Evaluate for malaria.
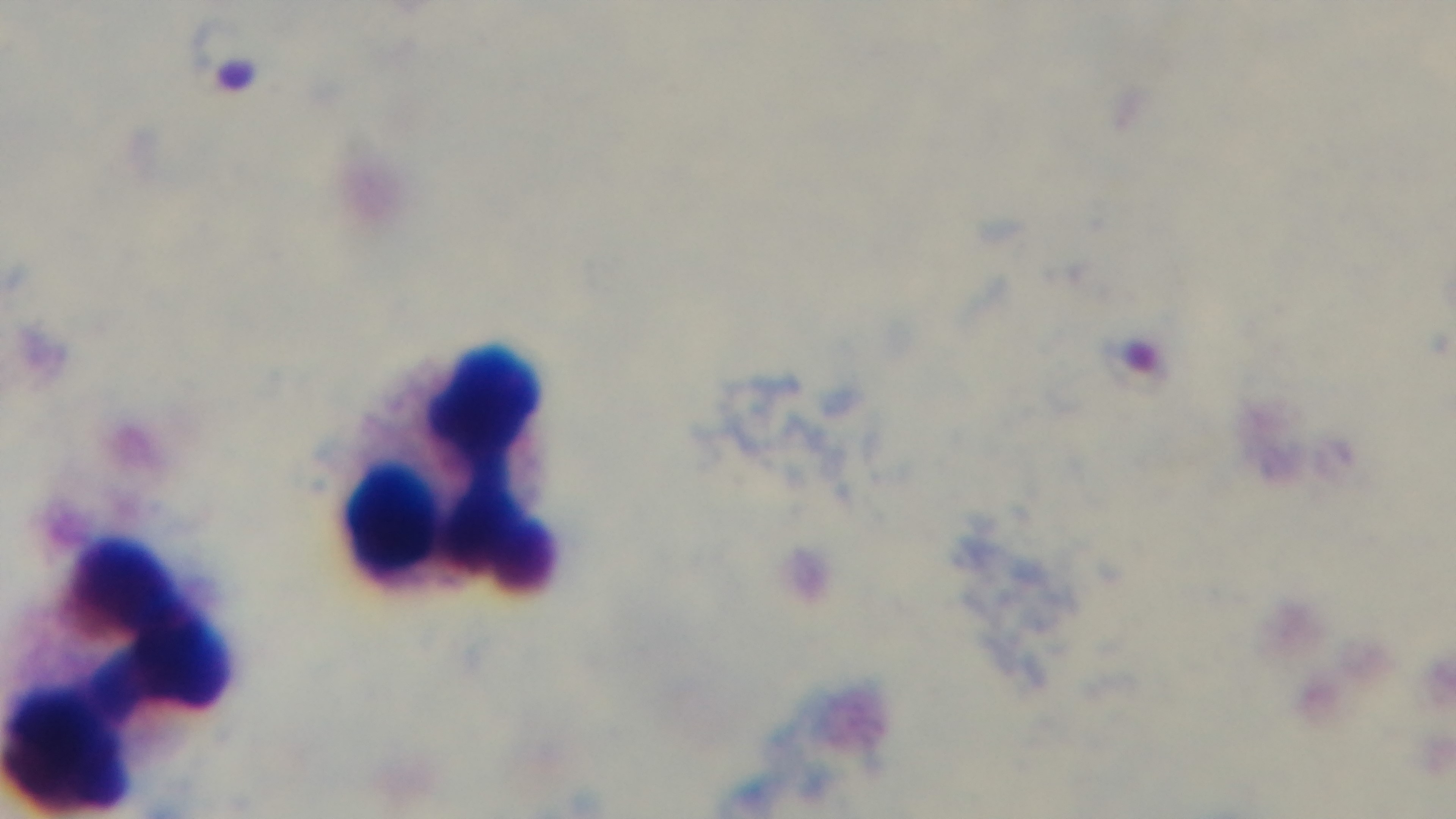
Infected.

stain: Giemsa
modality: light microscopy
objective: 100x oil immersion
preparation: thick blood film
field_of_view: one from the slide
capture: mounted 4K digital camera